Identify the cell.
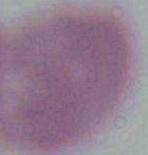
This is an erythrocyte.

1000x magnification. Photomicrograph.